Give the position of every Plasmodium parasite visible.
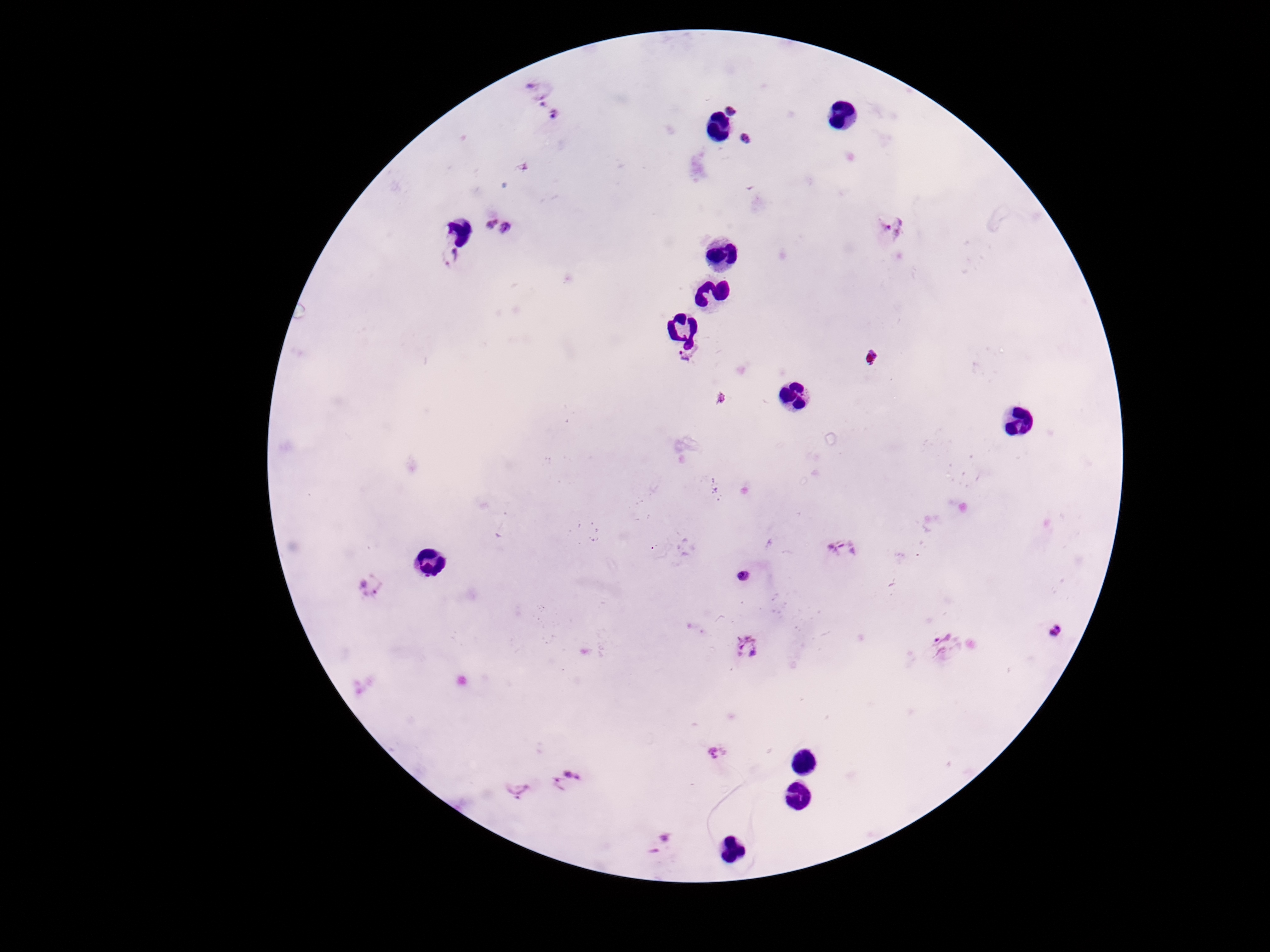
Approximate centers as {x, y} in pixels.
Plasmodium parasites: {537, 91}, {733, 105}, {556, 117}, {749, 141}, {496, 227}, {892, 228}, {449, 257}, {685, 360}, {844, 548}, {743, 576}, {375, 587}, {1056, 630}, {941, 643}, {747, 647}, {718, 753}, {568, 782}, {517, 790}, {664, 840}.

Summary:
  - Capture: smartphone camera through the microscope eyepiece
  - Preparation: thick peripheral-blood smear
  - Field of view: single
  - Patient malaria status: infected
  - Image size: 1270×952 pixels
  - Magnification: 100x
  - Stain: Giemsa